Classify this cell by malaria status.
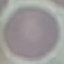

It is uninfected.

image type = automatically extracted cell patch, resized to 64 × 64 pixels
stain = Giemsa
capture = smartphone through the microscope eyepiece
preparation = thin blood film